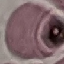

Summary:
  - Result: no malaria parasites detected
  - Capture: smartphone through the microscope eyepiece
  - Image type: cell patch, automatically extracted from a larger field of view and resized to 64 × 64 pixels
  - Preparation: thin blood film
  - Stain: Giemsa